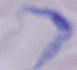

Summary:
  - Identification: trypanosome
  - Magnification: 1000x
  - Modality: micrograph